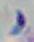
Summary:
  - Identification: Toxoplasma gondii
  - Magnification: 1000x
  - Modality: photomicrograph